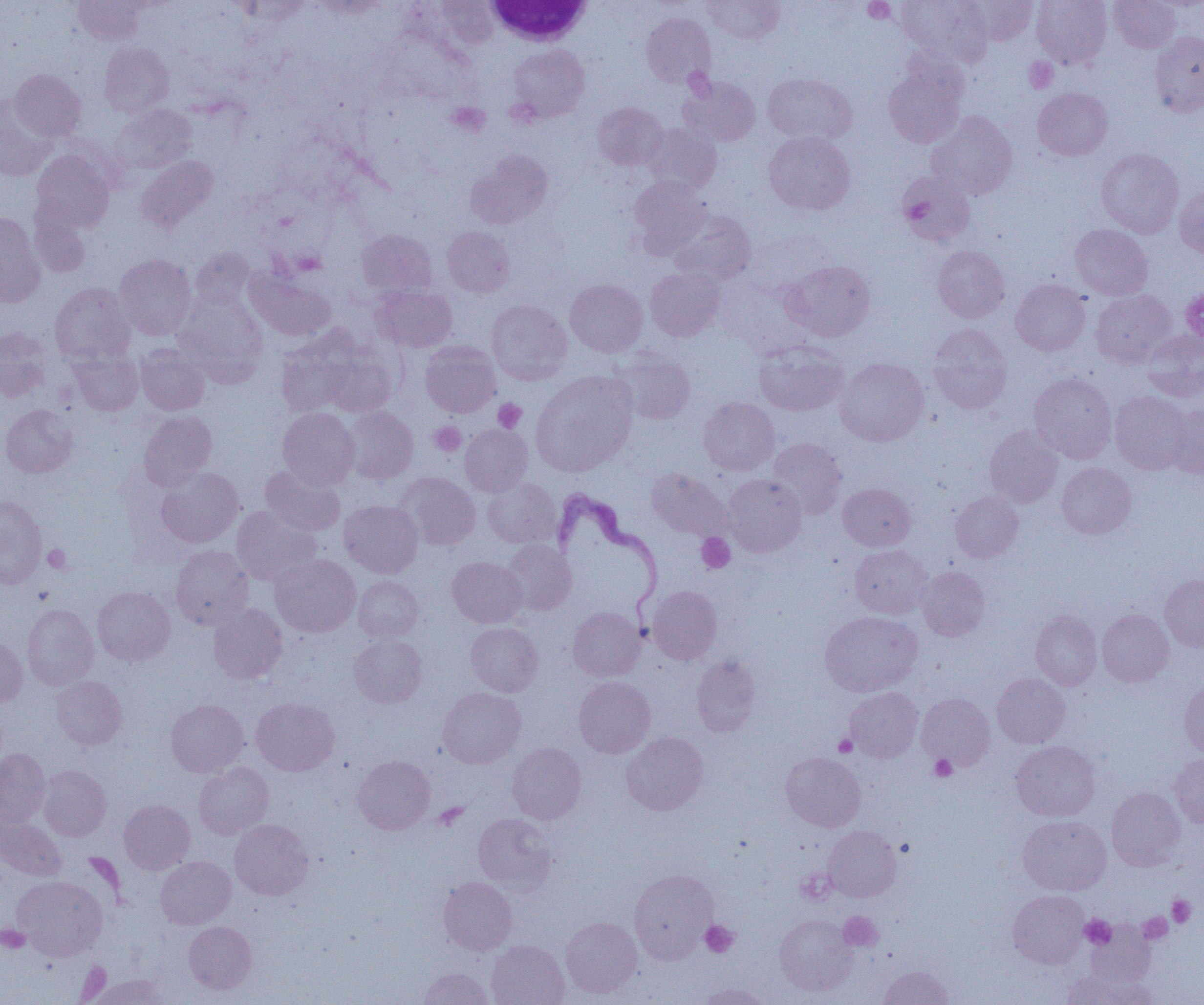
slide_level_diagnosis: Trypanosoma brucei
preparation: thin blood smear
field_of_view: single
modality: optical microscopy
image_size: 1204×1005 pixels
white_blood_cell_locations: 'approximate bounding boxes as named x1/y1/x2/y2 corners in pixels: (x1=483, y1=1, x2=593, y2=47)'
uninfected_red_blood_cell_locations: 'approximate bounding boxes as named x1/y1/x2/y2 corners in pixels: (x1=73, y1=0, x2=146, y2=45), (x1=427, y1=0, x2=503, y2=51), (x1=703, y1=0, x2=785, y2=43), (x1=895, y1=0, x2=992, y2=65), (x1=961, y1=0, x2=1038, y2=46), (x1=1032, y1=0, x2=1112, y2=69), (x1=1108, y1=0, x2=1180, y2=52), (x1=234, y1=1, x2=312, y2=28), (x1=641, y1=12, x2=715, y2=88), (x1=1149, y1=31, x2=1204, y2=117), (x1=100, y1=42, x2=174, y2=116), (x1=508, y1=44, x2=590, y2=122), (x1=883, y1=60, x2=968, y2=148), (x1=10, y1=70, x2=86, y2=141), (x1=762, y1=73, x2=857, y2=144), (x1=681, y1=76, x2=761, y2=146), (x1=1033, y1=87, x2=1113, y2=161), (x1=0, y1=95, x2=57, y2=180), (x1=593, y1=102, x2=667, y2=171), (x1=112, y1=104, x2=196, y2=173), (x1=926, y1=110, x2=1018, y2=200), (x1=643, y1=123, x2=721, y2=195), (x1=764, y1=132, x2=855, y2=214), (x1=1096, y1=148, x2=1184, y2=238), (x1=32, y1=149, x2=115, y2=233), (x1=464, y1=150, x2=553, y2=229), (x1=136, y1=156, x2=217, y2=232), (x1=897, y1=170, x2=976, y2=246), (x1=628, y1=178, x2=710, y2=258), (x1=1175, y1=185, x2=1204, y2=259), (x1=27, y1=201, x2=92, y2=279), (x1=670, y1=210, x2=756, y2=284), (x1=0, y1=213, x2=46, y2=307), (x1=1070, y1=224, x2=1153, y2=300), (x1=442, y1=226, x2=514, y2=297), (x1=356, y1=229, x2=437, y2=299), (x1=933, y1=245, x2=1010, y2=323), (x1=191, y1=248, x2=255, y2=311), (x1=114, y1=254, x2=196, y2=339), (x1=783, y1=260, x2=876, y2=341), (x1=246, y1=267, x2=336, y2=341), (x1=645, y1=268, x2=725, y2=341), (x1=565, y1=279, x2=648, y2=357), (x1=1011, y1=279, x2=1090, y2=355), (x1=50, y1=282, x2=135, y2=365), (x1=374, y1=286, x2=457, y2=352), (x1=1090, y1=290, x2=1176, y2=367), (x1=174, y1=291, x2=268, y2=384), (x1=486, y1=299, x2=572, y2=384), (x1=929, y1=324, x2=1012, y2=414), (x1=0, y1=328, x2=52, y2=402), (x1=274, y1=330, x2=365, y2=418), (x1=1142, y1=330, x2=1204, y2=401), (x1=753, y1=340, x2=849, y2=416), (x1=420, y1=341, x2=500, y2=418), (x1=135, y1=343, x2=209, y2=415), (x1=68, y1=347, x2=143, y2=416), (x1=314, y1=347, x2=398, y2=418), (x1=613, y1=352, x2=695, y2=424), (x1=836, y1=358, x2=928, y2=446), (x1=531, y1=371, x2=638, y2=476), (x1=1029, y1=373, x2=1117, y2=462), (x1=1110, y1=391, x2=1192, y2=474), (x1=698, y1=397, x2=779, y2=475), (x1=1, y1=404, x2=78, y2=478), (x1=1166, y1=405, x2=1204, y2=480), (x1=340, y1=406, x2=418, y2=484), (x1=277, y1=407, x2=360, y2=489), (x1=139, y1=411, x2=217, y2=491), (x1=460, y1=424, x2=532, y2=496), (x1=984, y1=425, x2=1064, y2=508), (x1=768, y1=438, x2=847, y2=518), (x1=1057, y1=463, x2=1136, y2=538), (x1=259, y1=465, x2=345, y2=536), (x1=157, y1=467, x2=244, y2=548), (x1=647, y1=468, x2=731, y2=541), (x1=396, y1=472, x2=480, y2=550), (x1=723, y1=474, x2=806, y2=556), (x1=483, y1=477, x2=561, y2=548), (x1=838, y1=483, x2=916, y2=551), (x1=950, y1=490, x2=1023, y2=562), (x1=0, y1=495, x2=48, y2=588), (x1=339, y1=500, x2=423, y2=578), (x1=232, y1=507, x2=321, y2=586), (x1=501, y1=539, x2=576, y2=616), (x1=850, y1=544, x2=932, y2=619), (x1=170, y1=546, x2=252, y2=630), (x1=271, y1=555, x2=360, y2=637), (x1=447, y1=556, x2=527, y2=627), (x1=917, y1=566, x2=990, y2=641), (x1=1160, y1=574, x2=1204, y2=651), (x1=354, y1=576, x2=424, y2=642), (x1=647, y1=586, x2=722, y2=664), (x1=92, y1=587, x2=175, y2=666), (x1=208, y1=603, x2=288, y2=684), (x1=22, y1=604, x2=98, y2=690), (x1=567, y1=607, x2=646, y2=681), (x1=1097, y1=609, x2=1174, y2=686), (x1=1031, y1=610, x2=1102, y2=690), (x1=820, y1=611, x2=922, y2=696), (x1=465, y1=622, x2=543, y2=697), (x1=348, y1=635, x2=427, y2=708), (x1=0, y1=636, x2=27, y2=707), (x1=691, y1=654, x2=761, y2=737), (x1=992, y1=673, x2=1070, y2=748), (x1=51, y1=675, x2=127, y2=749), (x1=574, y1=676, x2=655, y2=758), (x1=1179, y1=681, x2=1204, y2=757), (x1=845, y1=687, x2=922, y2=762), (x1=437, y1=688, x2=525, y2=768), (x1=917, y1=694, x2=995, y2=771), (x1=251, y1=697, x2=339, y2=776), (x1=165, y1=699, x2=249, y2=777), (x1=621, y1=732, x2=709, y2=815), (x1=1011, y1=741, x2=1100, y2=821), (x1=507, y1=743, x2=586, y2=824), (x1=0, y1=749, x2=50, y2=827), (x1=781, y1=752, x2=866, y2=831), (x1=353, y1=755, x2=435, y2=834), (x1=1169, y1=755, x2=1204, y2=829), (x1=194, y1=762, x2=274, y2=839), (x1=38, y1=765, x2=111, y2=841), (x1=1106, y1=787, x2=1185, y2=870), (x1=119, y1=799, x2=195, y2=874), (x1=473, y1=813, x2=557, y2=893), (x1=1018, y1=815, x2=1111, y2=895), (x1=0, y1=817, x2=67, y2=880), (x1=230, y1=819, x2=313, y2=900), (x1=823, y1=826, x2=901, y2=901), (x1=155, y1=856, x2=236, y2=929), (x1=629, y1=869, x2=717, y2=963), (x1=13, y1=875, x2=107, y2=960), (x1=438, y1=877, x2=517, y2=954), (x1=1008, y1=890, x2=1089, y2=968), (x1=774, y1=915, x2=857, y2=995), (x1=560, y1=917, x2=642, y2=998), (x1=184, y1=921, x2=257, y2=993), (x1=1086, y1=923, x2=1156, y2=987), (x1=486, y1=940, x2=569, y2=1005), (x1=879, y1=965, x2=954, y2=1005), (x1=418, y1=967, x2=494, y2=1005), (x1=1064, y1=969, x2=1154, y2=1005), (x1=88, y1=973, x2=172, y2=1004), (x1=695, y1=983, x2=775, y2=1005)'
trypanosoma_brucei_locations: 'approximate bounding boxes as named x1/y1/x2/y2 corners in pixels: (x1=553, y1=488, x2=664, y2=615)'
magnification: 1000x
platelet_locations: 'approximate bounding boxes as named x1/y1/x2/y2 corners in pixels: (x1=863, y1=0, x2=897, y2=23), (x1=1024, y1=57, x2=1058, y2=93), (x1=448, y1=103, x2=490, y2=136), (x1=493, y1=399, x2=526, y2=432), (x1=429, y1=422, x2=466, y2=457), (x1=696, y1=533, x2=735, y2=573), (x1=44, y1=545, x2=71, y2=573), (x1=834, y1=734, x2=857, y2=756), (x1=930, y1=754, x2=957, y2=781), (x1=434, y1=803, x2=469, y2=830), (x1=1167, y1=895, x2=1195, y2=927), (x1=1144, y1=904, x2=1183, y2=935), (x1=839, y1=912, x2=883, y2=951), (x1=1138, y1=913, x2=1172, y2=944), (x1=1080, y1=915, x2=1116, y2=949), (x1=700, y1=921, x2=738, y2=957), (x1=0, y1=925, x2=31, y2=953)'